Locate every Plasmodium parasite.
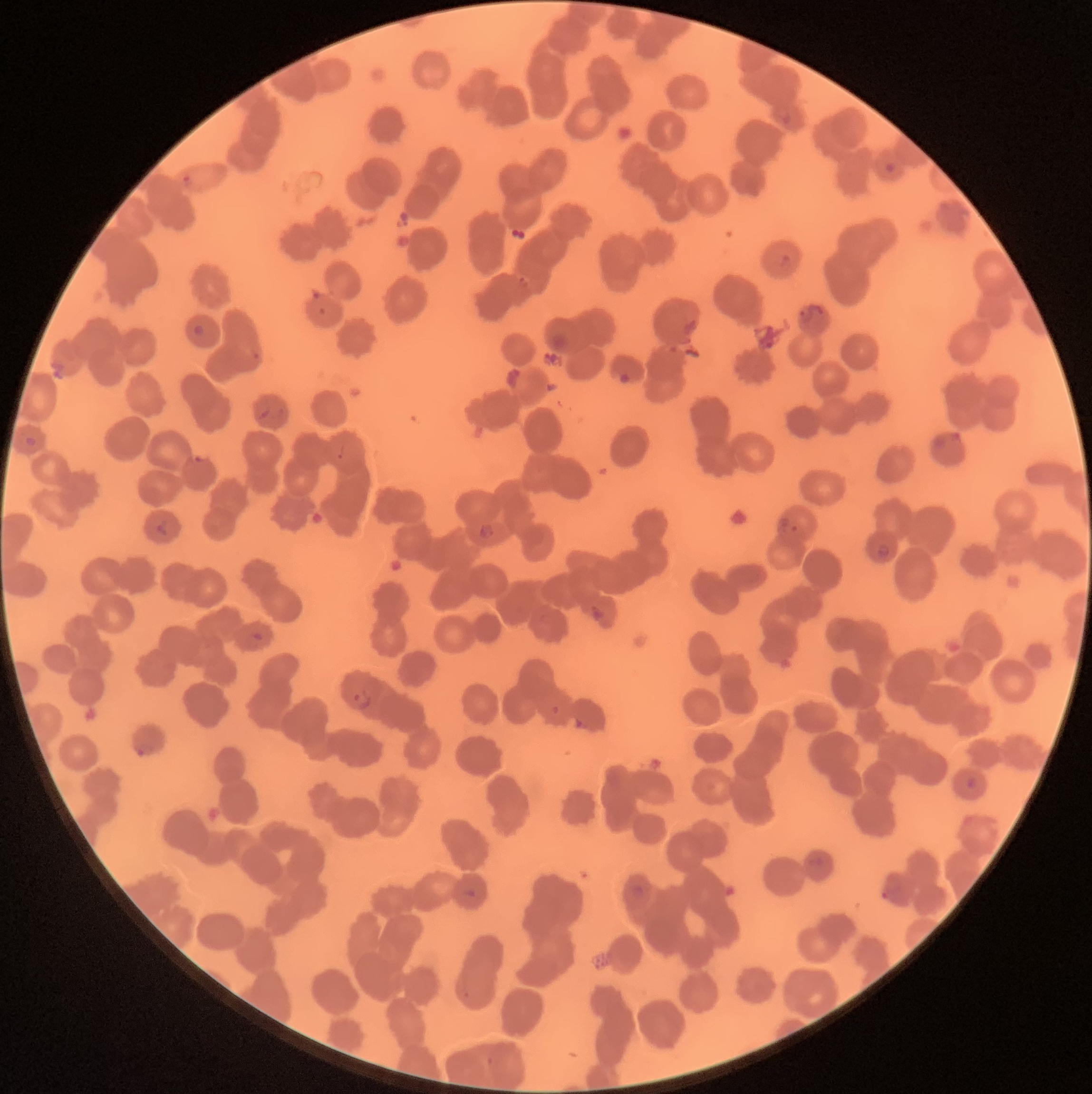
Approximate bounding boxes as [x1, y1, x2, y2] in pixels.
Plasmodium parasites: [774, 107, 792, 125], [885, 162, 895, 173], [779, 253, 792, 273], [796, 306, 813, 324], [192, 325, 205, 337], [929, 431, 967, 467], [25, 436, 37, 447], [777, 516, 799, 536], [155, 520, 169, 536], [476, 524, 496, 539], [876, 543, 890, 558], [589, 603, 605, 623], [246, 631, 263, 648], [351, 690, 372, 711], [133, 741, 154, 758], [966, 776, 976, 789], [812, 856, 826, 869], [881, 885, 909, 906], [464, 888, 476, 899].

Image is 1092×1094 pixels. Light microscopy. The red blood cells show rouleaux formation. Thin blood film.